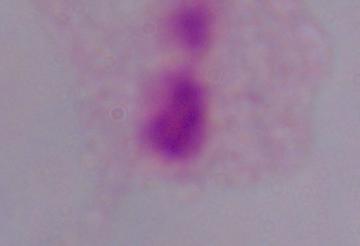
1000x magnification. A trichomonad is seen. Photomicrograph.